Assess this cell for malaria.
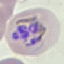

It is parasitized.

Summary:
  - Capture: smartphone through the microscope eyepiece
  - Image type: cell patch, automatically extracted from a larger field of view and resized to 64 × 64 pixels
  - Stain: Giemsa
  - Preparation: thin blood film